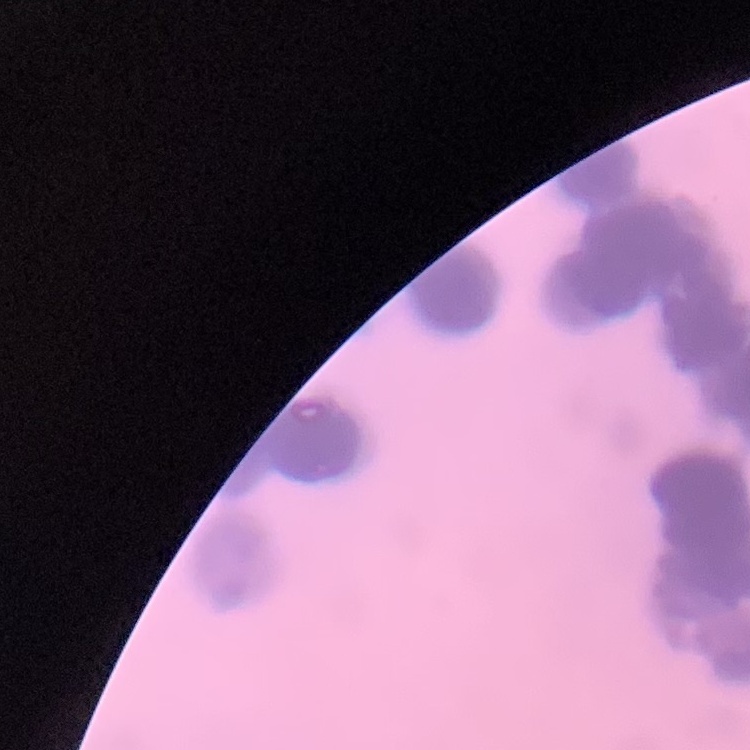
erythrocyte_morphology: rouleaux formation
preparation: thin blood film
stain: Field's or Giemsa
image_type: one tile cut from a larger photomicrograph